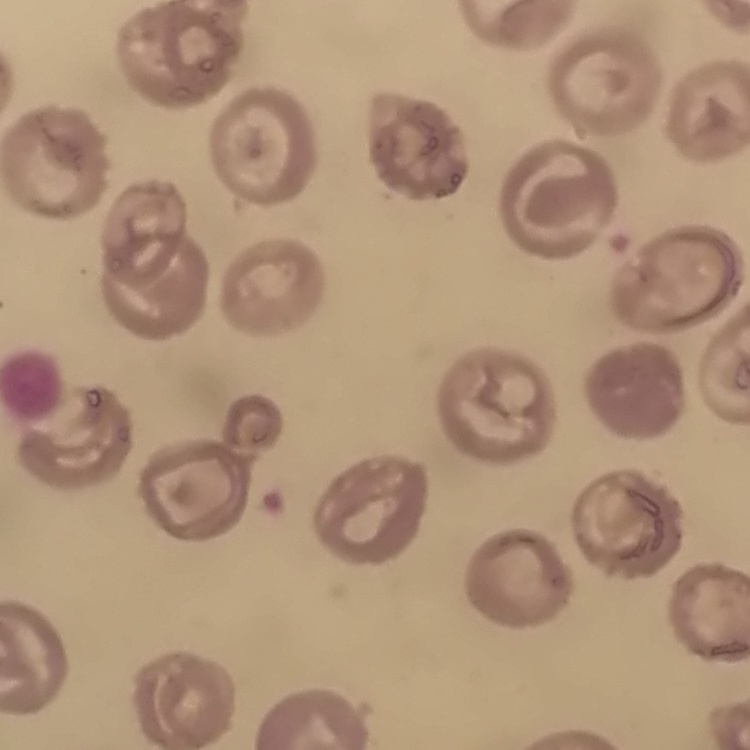

The erythrocytes exhibit no rouleaux formation. Thin blood smear. Square crop of a larger photomicrograph. Stained with either Field's or Giemsa.